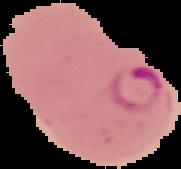
result = Plasmodium parasites detected
preparation = thin blood film
image size = 181×169 pixels
image type = cell region segmented out of the field of view; surrounding area masked to black